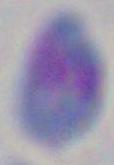 Toxoplasma gondii is seen. 1000x magnification. Micrograph.